Give the position of every Plasmodium parasite visible.
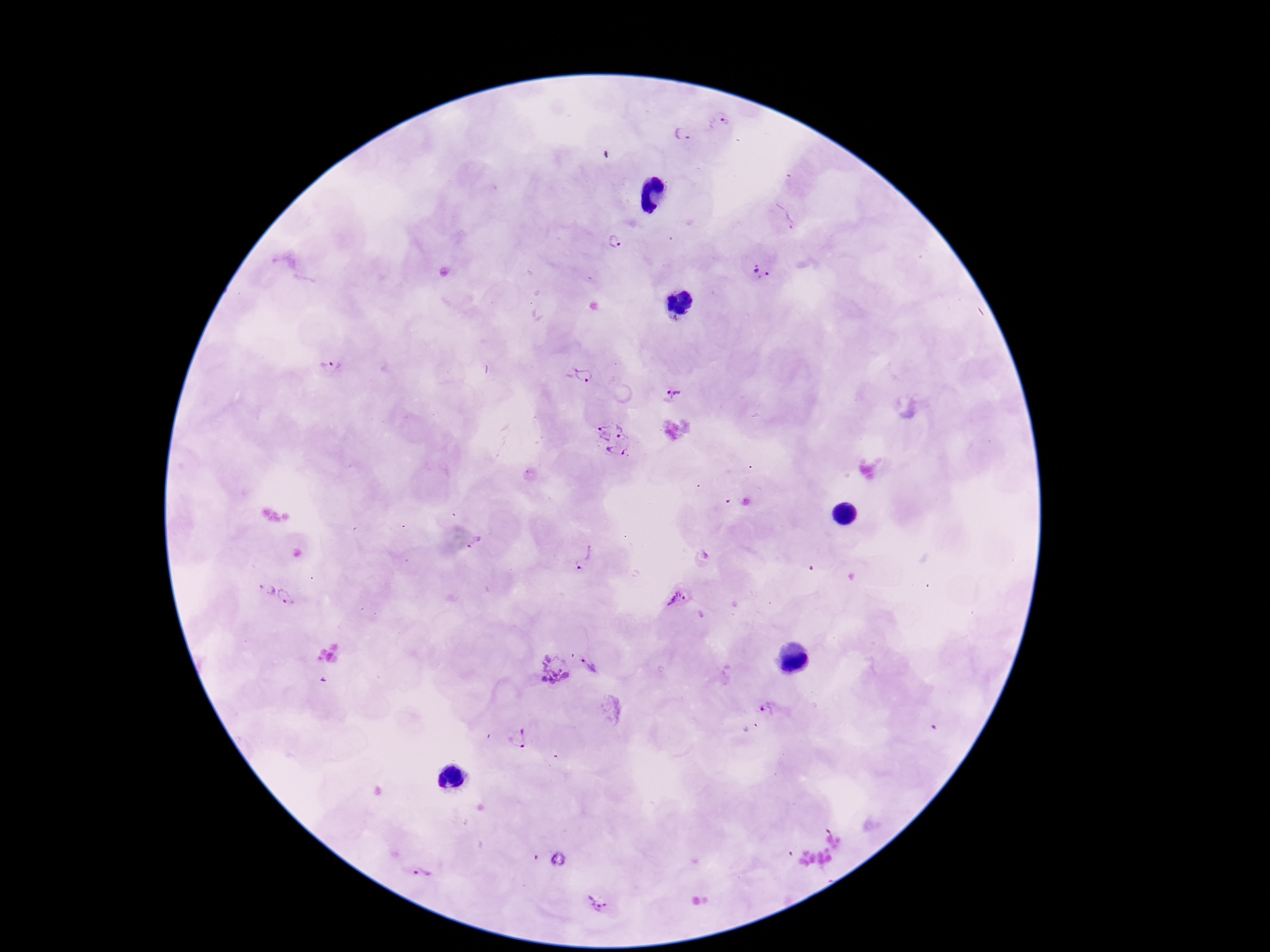

Approximate centers as (x, y) in pixels.
Plasmodium parasites: (723, 122), (684, 133), (785, 219), (616, 241), (760, 271), (329, 370), (583, 375), (671, 394), (614, 441), (474, 542), (584, 558), (262, 585), (289, 596), (680, 596), (593, 664), (555, 669), (770, 711), (520, 739), (421, 872), (600, 903).

patient malaria status = infected
preparation = thick peripheral-blood smear
field of view = single
capture = smartphone camera through the microscope eyepiece
image size = 1270×952 pixels
magnification = 100x
stain = Giemsa